Point out each Plasmodium parasite and each leukocyte.
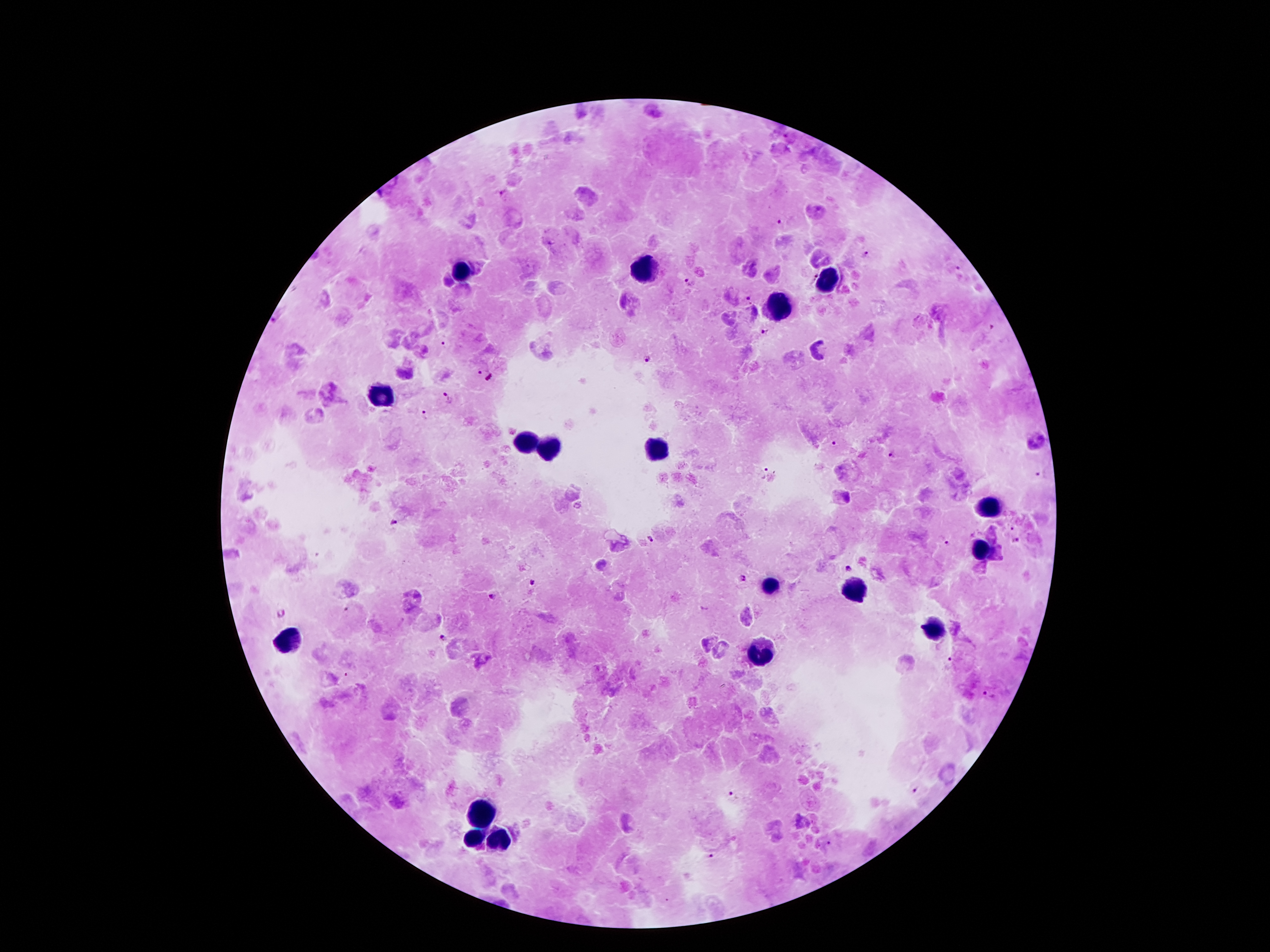

Approximate centers as {x, y} in pixels.
Plasmodium parasites: {502, 191}, {779, 221}, {867, 254}, {958, 267}, {814, 277}, {688, 280}, {749, 299}, {993, 326}, {764, 332}, {444, 344}, {648, 358}, {479, 372}, {490, 378}, {448, 396}, {424, 414}, {835, 444}, {892, 454}, {763, 472}, {1037, 473}, {394, 523}, {1012, 527}, {653, 540}, {1015, 542}, {946, 544}, {847, 567}, {742, 580}, {532, 583}, {493, 597}, {345, 609}, {281, 612}, {443, 639}, {950, 660}, {345, 674}, {987, 694}, {915, 790}, {733, 793}, {828, 844}, {711, 855}.
Leukocytes: {641, 267}, {462, 272}, {827, 284}, {779, 308}, {380, 398}, {526, 444}, {551, 449}, {656, 450}, {986, 511}, {980, 551}, {771, 586}, {855, 591}, {936, 629}, {290, 641}, {760, 655}, {482, 814}, {501, 838}, {475, 841}.

Summary:
  - Magnification: 100x
  - Field of view: single
  - Stain: Giemsa
  - Image size: 1270×952 pixels
  - Capture: smartphone through the microscope eyepiece
  - Patient malaria status: positive for Plasmodium falciparum
  - Preparation: thick blood smear